Comment on the morphology of the erythrocytes.
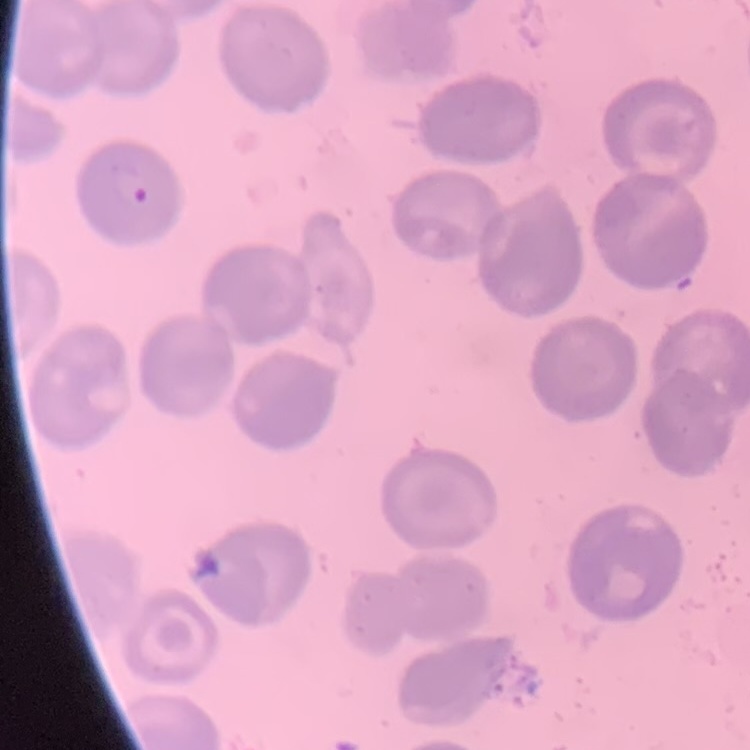
No rouleaux formation.

stain: Field's or Giemsa
preparation: thin peripheral smear
image_type: one tile cut from a larger photomicrograph